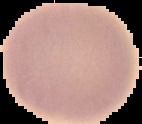

{
  "image_size": "142×124 pixels",
  "malaria_status": "uninfected",
  "preparation": "thin blood film",
  "image_type": "segmented cell region on a black background"
}